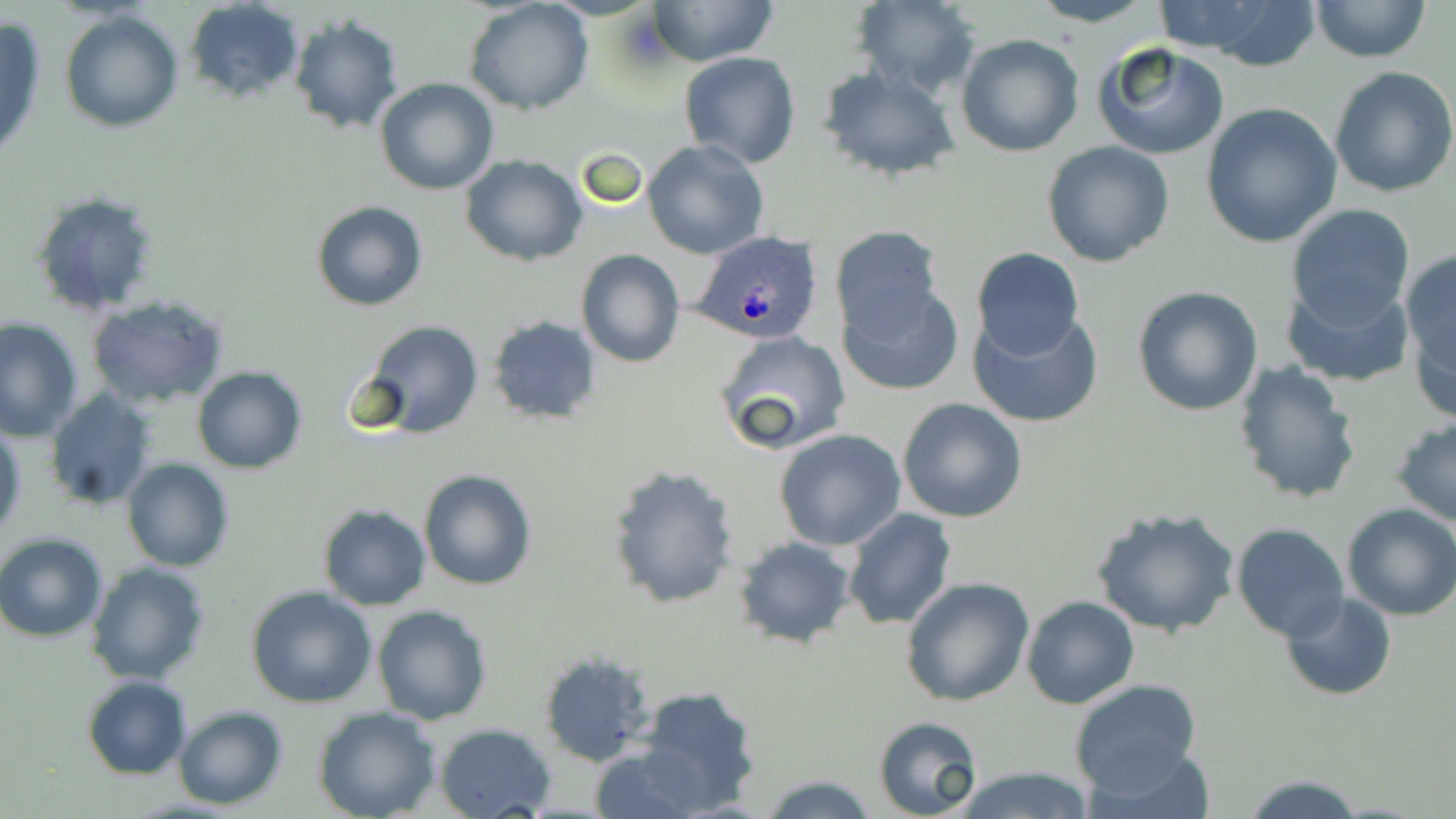

plasmodium_ovale_infected_red_blood_cell_locations: 'approximate bounding boxes as named x1/y1/x2/y2 corners in pixels: (x1=688, y1=231, x2=822, y2=347)'
slide_level_diagnosis: Plasmodium ovale
uninfected_red_blood_cell_locations: 'approximate bounding boxes as named x1/y1/x2/y2 corners in pixels: (x1=645, y1=0, x2=779, y2=66), (x1=851, y1=0, x2=982, y2=98), (x1=1027, y1=0, x2=1162, y2=27), (x1=1308, y1=0, x2=1433, y2=62), (x1=184, y1=1, x2=305, y2=103), (x1=465, y1=1, x2=594, y2=116), (x1=1149, y1=1, x2=1323, y2=71), (x1=60, y1=10, x2=184, y2=132), (x1=287, y1=15, x2=403, y2=135), (x1=0, y1=18, x2=48, y2=167), (x1=955, y1=33, x2=1084, y2=157), (x1=1093, y1=42, x2=1231, y2=162), (x1=680, y1=52, x2=800, y2=168), (x1=820, y1=65, x2=961, y2=183), (x1=1329, y1=66, x2=1456, y2=197), (x1=373, y1=77, x2=499, y2=195), (x1=1200, y1=102, x2=1344, y2=249), (x1=642, y1=139, x2=769, y2=259), (x1=1042, y1=141, x2=1174, y2=268), (x1=462, y1=155, x2=588, y2=267), (x1=30, y1=190, x2=163, y2=317), (x1=312, y1=201, x2=426, y2=311), (x1=1286, y1=204, x2=1415, y2=327), (x1=830, y1=226, x2=945, y2=340), (x1=972, y1=247, x2=1084, y2=357), (x1=576, y1=249, x2=684, y2=367), (x1=1399, y1=250, x2=1456, y2=412), (x1=1284, y1=280, x2=1413, y2=388), (x1=837, y1=283, x2=962, y2=395), (x1=1132, y1=285, x2=1263, y2=416), (x1=86, y1=294, x2=229, y2=408), (x1=970, y1=310, x2=1103, y2=428), (x1=487, y1=316, x2=600, y2=424), (x1=0, y1=317, x2=83, y2=440), (x1=358, y1=320, x2=484, y2=438), (x1=715, y1=330, x2=851, y2=455), (x1=1233, y1=361, x2=1364, y2=505), (x1=191, y1=365, x2=307, y2=473), (x1=45, y1=388, x2=157, y2=511), (x1=898, y1=397, x2=1027, y2=522), (x1=1391, y1=416, x2=1456, y2=527), (x1=0, y1=422, x2=25, y2=544), (x1=774, y1=429, x2=907, y2=551), (x1=121, y1=458, x2=233, y2=571), (x1=607, y1=464, x2=740, y2=611), (x1=418, y1=468, x2=537, y2=591), (x1=1340, y1=503, x2=1456, y2=621), (x1=317, y1=505, x2=432, y2=610), (x1=1090, y1=505, x2=1240, y2=639), (x1=842, y1=508, x2=956, y2=630), (x1=1236, y1=516, x2=1456, y2=634), (x1=1232, y1=524, x2=1349, y2=642), (x1=0, y1=533, x2=108, y2=641), (x1=732, y1=536, x2=856, y2=650), (x1=86, y1=561, x2=209, y2=683), (x1=902, y1=576, x2=1035, y2=706), (x1=245, y1=586, x2=377, y2=708), (x1=1281, y1=591, x2=1396, y2=700), (x1=1022, y1=595, x2=1140, y2=710), (x1=372, y1=605, x2=492, y2=726), (x1=539, y1=650, x2=653, y2=766), (x1=81, y1=675, x2=191, y2=780), (x1=1068, y1=679, x2=1203, y2=795), (x1=633, y1=685, x2=763, y2=812), (x1=173, y1=706, x2=288, y2=808), (x1=315, y1=708, x2=440, y2=819), (x1=872, y1=715, x2=984, y2=819), (x1=433, y1=722, x2=556, y2=818), (x1=585, y1=741, x2=708, y2=818), (x1=952, y1=765, x2=1095, y2=819), (x1=1240, y1=773, x2=1365, y2=817), (x1=758, y1=774, x2=879, y2=817)'
image_size: 1456×819 pixels
stain: May-Grünwald-Giemsa
magnification: 1000x
field_of_view: one of a larger specimen
preparation: thin blood film
modality: light microscopy